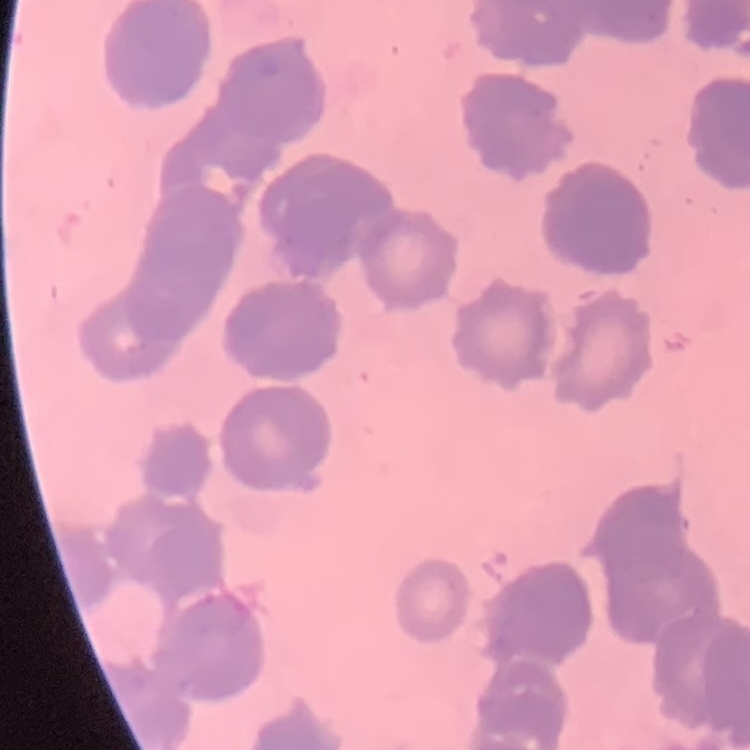

Summary:
  - Erythrocyte morphology: rouleaux formation
  - Image type: one tile cut from a larger photomicrograph
  - Preparation: thin peripheral smear
  - Stain: Field's or Giemsa